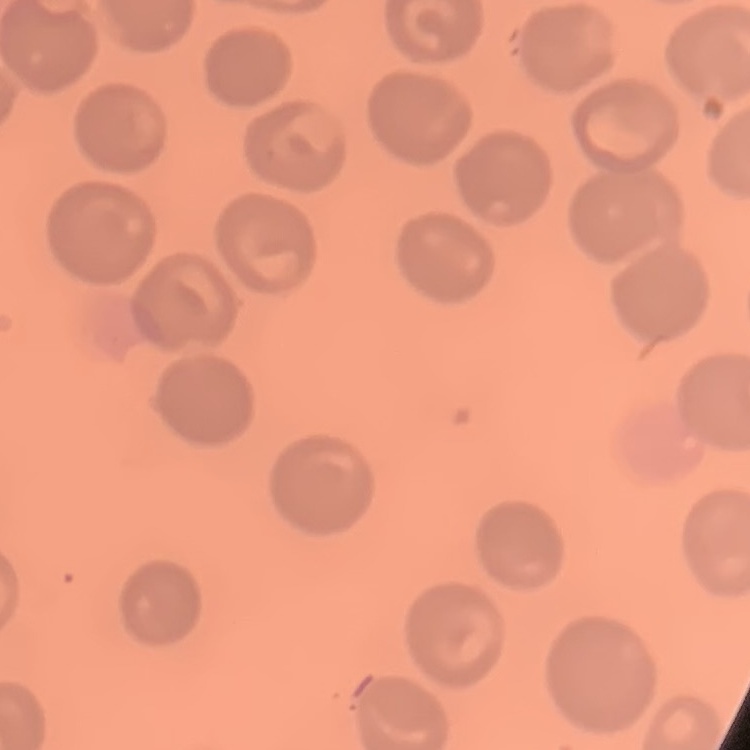
Summary:
  - Red blood cell morphology: no rouleaux formation
  - Preparation: thin blood smear
  - Image type: square crop of a larger photomicrograph
  - Stain: Field's or Giemsa